Describe the morphology of the erythrocytes.
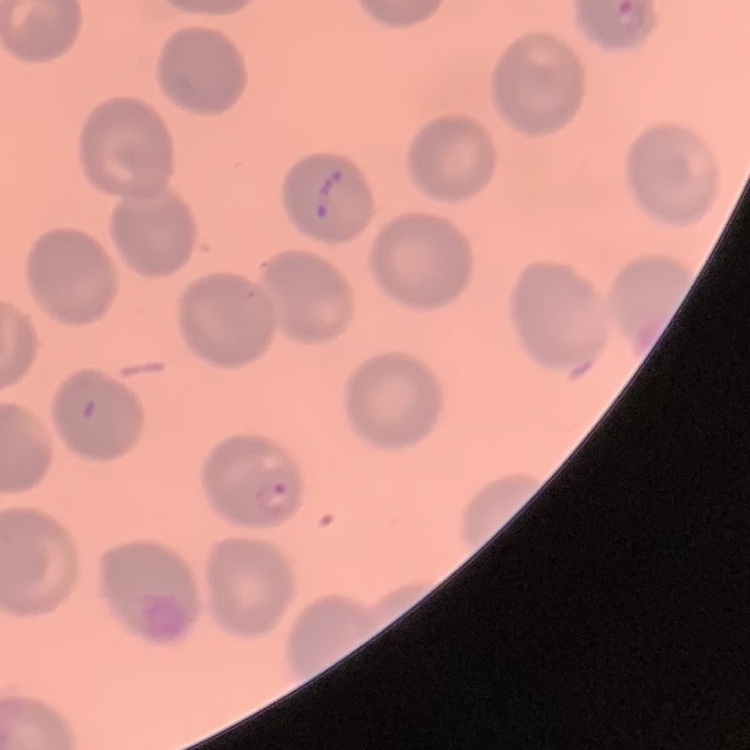

They show no rouleaux formation.

Field's or Giemsa stain. Thin blood smear. Square crop of a larger photomicrograph.